State which parasite is depicted.
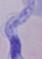

This is a trypanosome.

Photomicrograph. 1000x magnification.